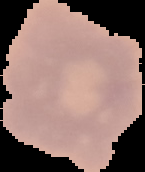
From a thin blood film. Image is 145×172 pixels. Malaria status: uninfected. The area outside the segmented cell region is set to black.